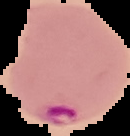

result = malaria parasites identified
preparation = thin blood film
image type = cell region segmented out of the field of view; surrounding area masked to black
image size = 130×136 pixels